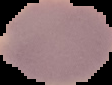

Summary:
  - Result: no Plasmodium parasites seen
  - Image size: 112×85 pixels
  - Image type: cell region segmented out of the field of view; surrounding area masked to black
  - Preparation: thin blood film